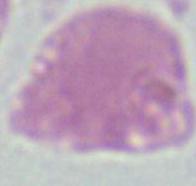

Summary:
  - Modality: micrograph
  - Magnification: 1000x
  - Identification: red blood cell